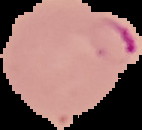
{
  "preparation": "thin blood smear",
  "malaria_status": "parasitized",
  "image_size": "142×130 pixels",
  "image_type": "cell region segmented out of the field of view; surrounding area masked to black"
}